Look for parasitized red blood cells.
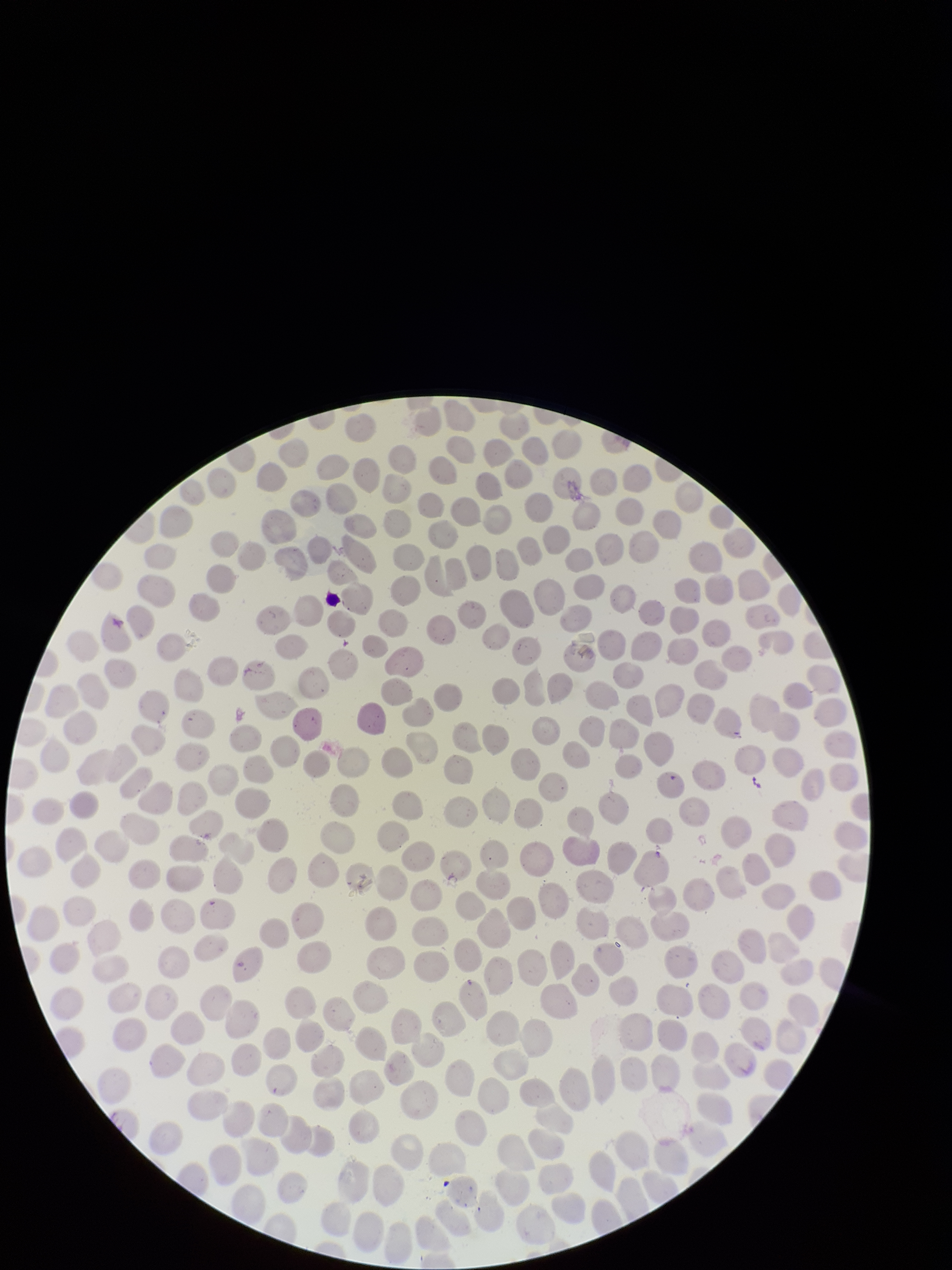
None seen.

Preparation: thin. One field from this slide. Smartphone photograph taken through the eyepiece of a microscope. Stained with Giemsa. Patient malaria status: negative. Image is 952×1270 pixels. Parasitized red blood cell count: 0. Red blood cell count: 287.